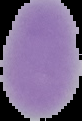

Malaria status: uninfected. From a thin blood smear. Image is 82×121 pixels. Segmented cell region on a black background.